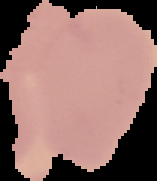

Summary:
  - Image size: 157×181 pixels
  - Image type: cell region segmented out of the field of view; surrounding area masked to black
  - Preparation: thin blood smear
  - Malaria status: uninfected